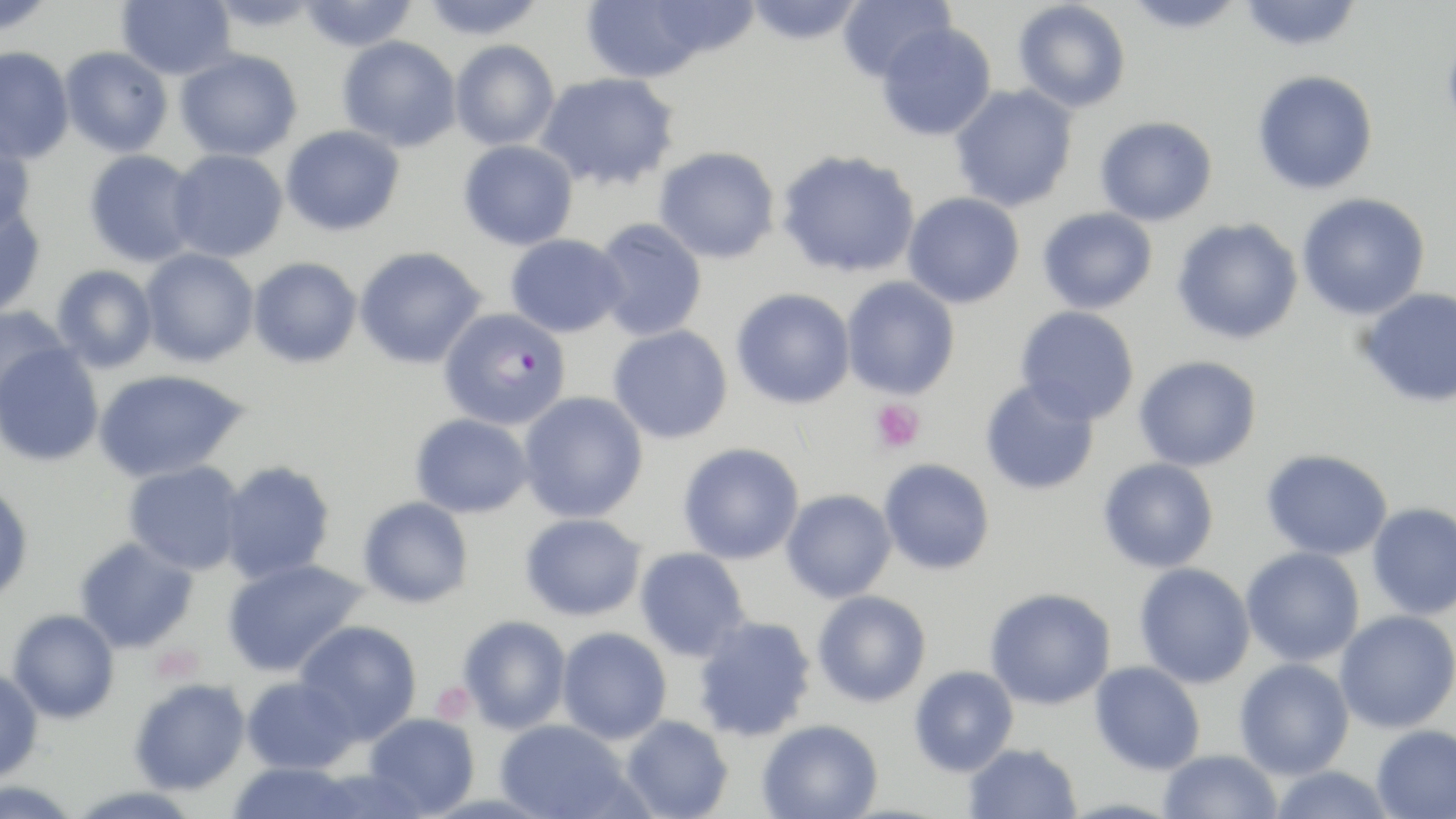

Summary:
  - Coordinate format: approximate bounding boxes as (x1,y1)-(x2,y2) corner pairs in pixels
  - Plasmodium falciparum-infected red blood cell locations: (439,308)-(570,431)
  - Uninfected red blood cell locations: (0,0)-(59,36), (116,0)-(235,80), (298,0)-(420,52), (419,0)-(548,40), (581,0)-(711,84), (645,0)-(761,61), (837,0)-(955,85), (1013,0)-(1131,113), (1122,0)-(1248,34), (1239,0)-(1363,52), (742,1)-(866,46), (1441,21)-(1456,147), (877,23)-(997,142), (337,36)-(462,152), (450,41)-(560,151), (0,47)-(75,165), (59,47)-(173,157), (175,50)-(302,161), (1252,70)-(1378,195), (535,72)-(681,193), (949,83)-(1080,212), (1094,116)-(1217,226), (281,125)-(405,237), (0,132)-(36,240), (458,140)-(578,251), (654,146)-(780,264), (83,149)-(201,268), (167,149)-(289,262), (776,150)-(920,279), (902,192)-(1025,309), (1296,193)-(1430,320), (0,206)-(47,318), (1037,207)-(1158,314), (1171,217)-(1304,345), (592,218)-(707,341), (505,234)-(627,338), (354,246)-(487,369), (139,248)-(259,367), (248,257)-(362,369), (52,264)-(159,373), (841,275)-(960,400), (1357,287)-(1456,408), (731,288)-(856,410), (0,304)-(71,413), (1015,305)-(1139,426), (608,324)-(733,444), (1,342)-(104,467), (1133,356)-(1262,471), (92,369)-(249,483), (980,379)-(1099,495), (518,391)-(649,523), (410,413)-(534,519), (678,443)-(804,564), (1261,449)-(1392,560), (1098,457)-(1219,573), (879,459)-(995,575), (122,460)-(246,576), (219,460)-(336,584), (0,483)-(33,604), (781,489)-(897,603), (358,496)-(474,609), (1367,502)-(1456,620), (520,513)-(645,622), (74,537)-(199,654), (634,546)-(750,662), (1240,547)-(1365,666), (222,557)-(369,678), (1134,562)-(1255,688), (985,588)-(1115,710), (813,590)-(932,708), (7,609)-(119,723), (1335,610)-(1456,733), (458,615)-(571,734), (692,615)-(817,741), (294,620)-(422,744), (557,627)-(672,744), (1234,657)-(1354,780), (1090,661)-(1205,775), (909,665)-(1019,777), (0,668)-(44,783), (241,676)-(360,774), (129,678)-(251,795), (364,712)-(480,817), (621,715)-(733,819), (495,719)-(634,819), (757,720)-(883,819), (1371,724)-(1456,818), (964,743)-(1083,819), (1158,749)-(1283,819), (226,762)-(364,819), (1268,765)-(1396,819), (306,768)-(430,819), (0,779)-(84,819)
  - Platelet locations: (871,398)-(925,453), (152,644)-(203,684), (431,681)-(476,724)
  - Slide-level diagnosis: Plasmodium falciparum
  - Field of view: one of a larger specimen
  - Preparation: thin blood smear
  - Magnification: 1000x
  - Image size: 1456×819 pixels
  - Modality: optical microscopy
  - Stain: May-Grünwald-Giemsa